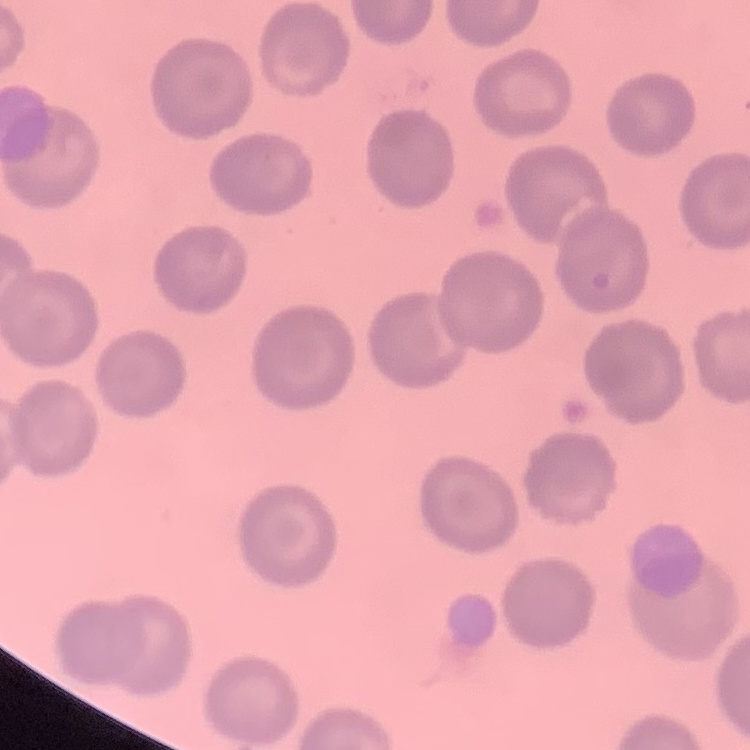
Summary:
  - Erythrocyte morphology: no rouleaux formation
  - Stain: Field's or Giemsa
  - Image type: one tile cut from a larger photomicrograph
  - Preparation: thin blood film